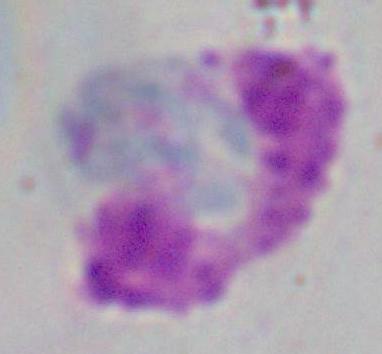
magnification = 1000x
modality = micrograph
identification = white blood cell